Report the malaria status of this cell.
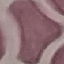

Uninfected.

{
  "image_type": "automatically extracted cell patch, resized to 64 × 64 pixels",
  "preparation": "thin blood smear",
  "capture": "smartphone through the microscope eyepiece",
  "stain": "Giemsa"
}